Give the position of every Plasmodium parasite visible.
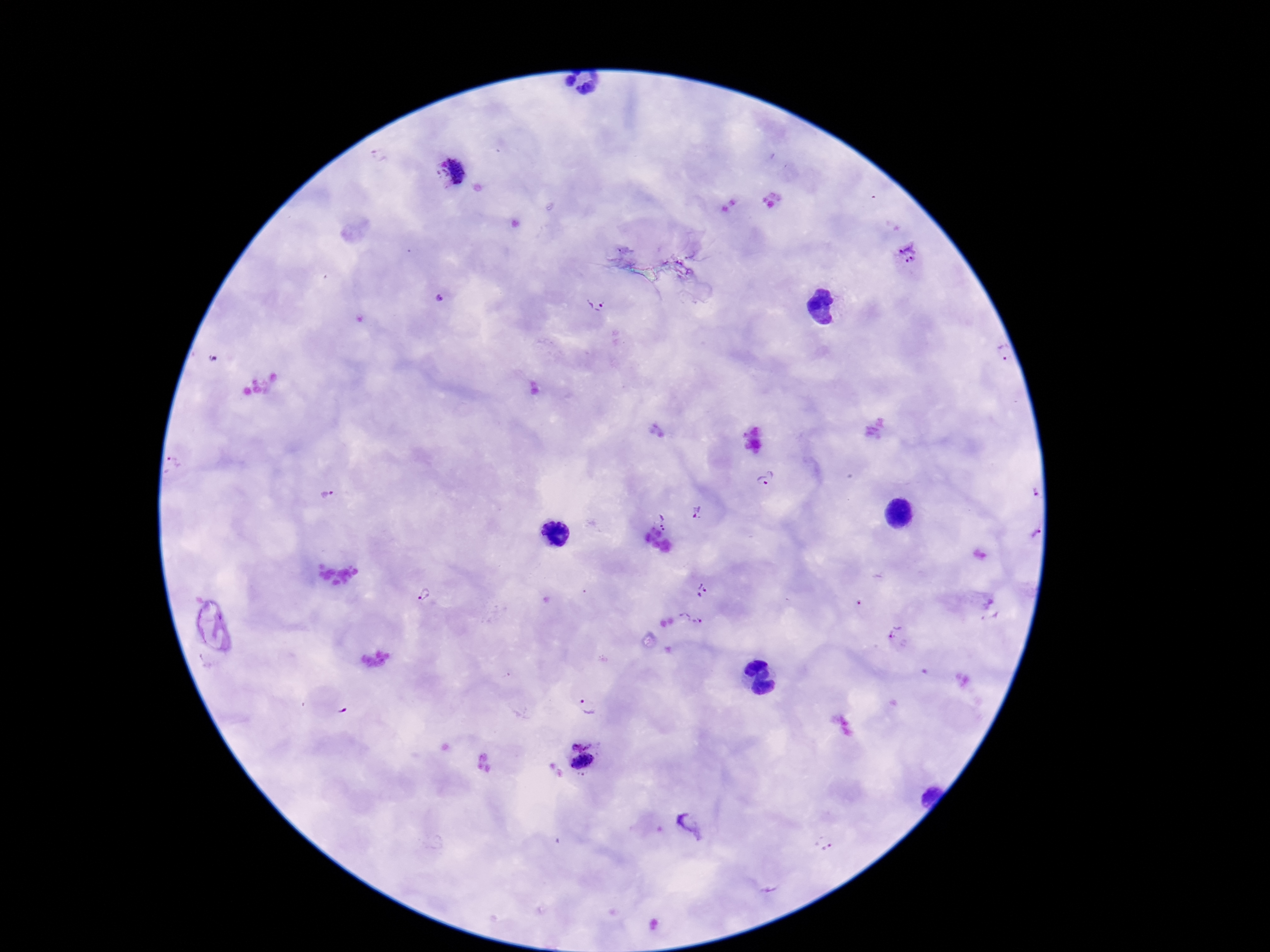

Approximate centers as {x, y} in pixels.
Plasmodium parasites: {450, 173}, {910, 252}, {599, 303}, {1000, 352}, {213, 359}, {766, 479}, {1027, 485}, {327, 490}, {701, 513}, {663, 523}, {1025, 531}, {703, 590}, {425, 593}, {689, 619}, {897, 635}, {588, 700}, {581, 738}, {582, 763}, {691, 825}, {826, 843}.

Summary:
  - Stain: Giemsa
  - Image size: 1270×952 pixels
  - Field of view: one from this slide
  - Capture: smartphone camera through the microscope eyepiece
  - Patient malaria status: infected
  - Magnification: 100x
  - Preparation: thick blood smear